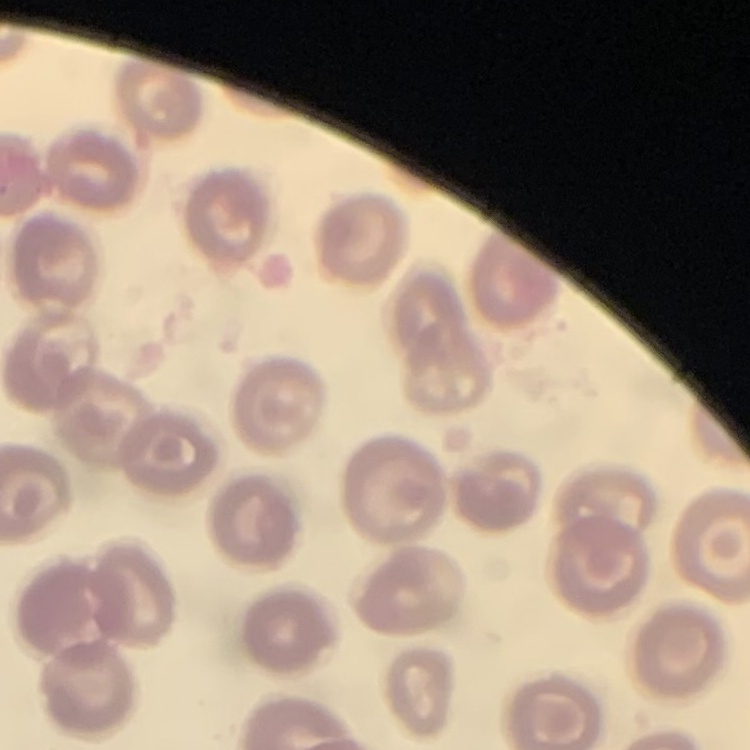
erythrocyte morphology = no rouleaux formation
preparation = thin blood film
image type = one tile cut from a larger photomicrograph
stain = Field's or Giemsa